State the blood parasite species.
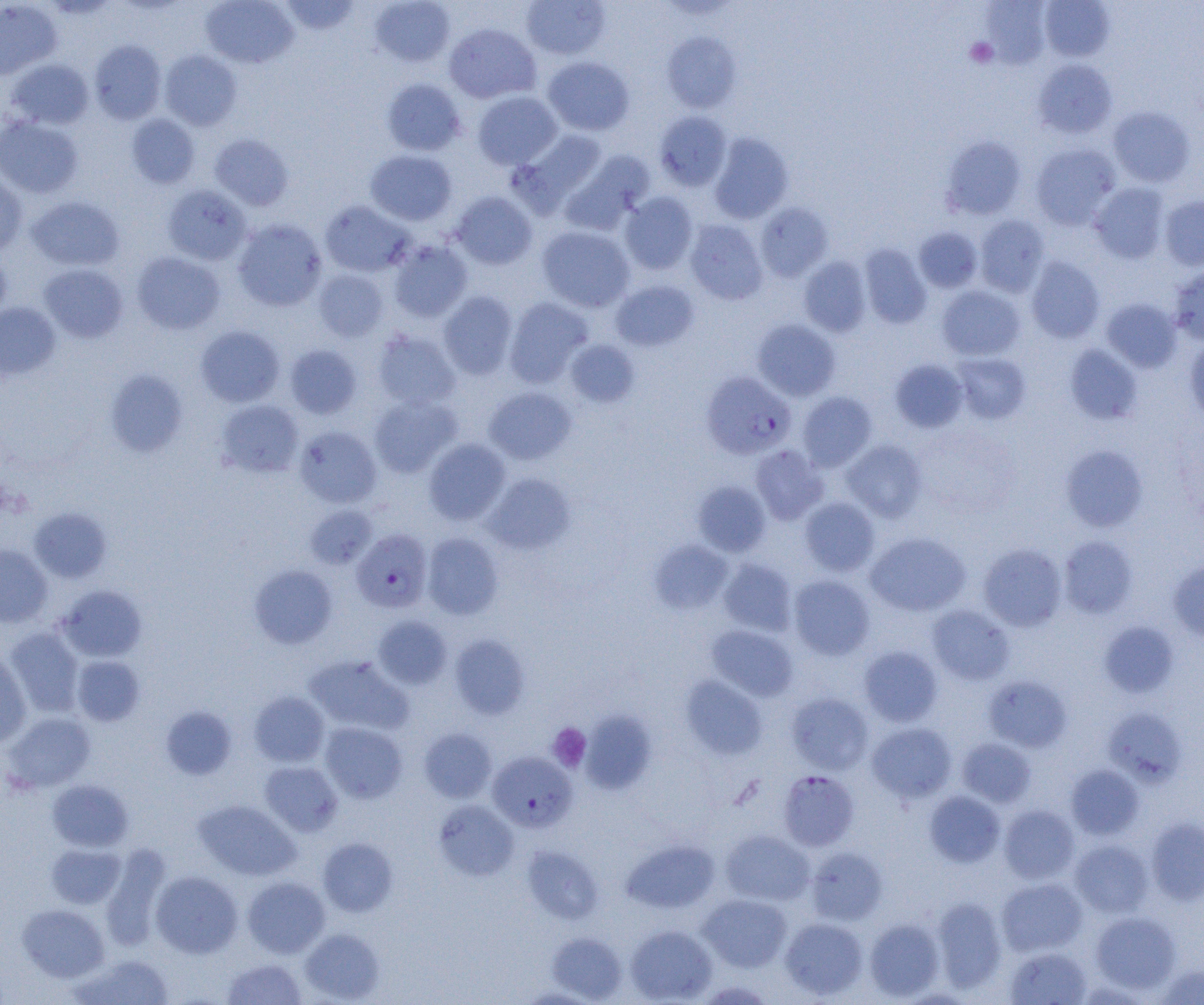

Plasmodium falciparum.

Approximate bounding boxes as (x1,y1)-(x2,y2) corner pairs in pixels. Uninfected red blood cell locations: (201,0)-(299,68), (280,0)-(360,36), (370,0)-(455,67), (521,0)-(611,60), (1039,0)-(1115,61), (0,1)-(61,79), (980,1)-(1052,69), (444,23)-(541,104), (662,31)-(741,113), (89,40)-(166,124), (159,50)-(242,130), (542,56)-(634,136), (5,58)-(94,130), (1033,59)-(1117,138), (381,78)-(466,156), (472,91)-(562,170), (1108,105)-(1195,187), (655,111)-(732,191), (126,113)-(200,189), (0,116)-(83,198), (515,128)-(608,209), (709,133)-(793,223), (210,134)-(293,211), (941,136)-(1026,219), (1030,144)-(1120,229), (365,149)-(457,226), (563,151)-(655,231), (0,171)-(27,255), (1089,183)-(1170,264), (162,184)-(251,265), (450,191)-(537,270), (619,191)-(698,275), (1160,195)-(1204,271), (26,196)-(124,272), (320,201)-(414,277), (755,202)-(833,282), (974,215)-(1050,296), (233,219)-(328,311), (685,219)-(768,305), (536,226)-(635,312), (913,226)-(983,293), (389,240)-(473,322), (859,243)-(931,328), (0,250)-(11,322), (132,252)-(225,335), (798,256)-(872,337), (1026,256)-(1104,343), (39,264)-(128,342), (1168,266)-(1204,345), (314,269)-(388,342), (610,279)-(699,352), (936,285)-(1025,361), (438,291)-(518,379), (504,297)-(593,387), (1101,298)-(1182,373), (0,302)-(61,380), (752,319)-(840,401), (196,325)-(284,407), (372,329)-(460,410), (1184,336)-(1204,422), (565,339)-(640,408), (285,344)-(363,419), (1064,344)-(1143,424), (951,353)-(1031,424), (890,360)-(968,433), (105,369)-(188,457), (483,387)-(577,465), (797,391)-(877,471), (369,394)-(461,477), (216,399)-(304,478), (294,425)-(382,508), (423,438)-(511,525), (841,439)-(927,522), (750,444)-(828,525), (1060,445)-(1148,532), (483,472)-(576,555), (693,480)-(771,557), (799,497)-(880,576), (304,504)-(378,569), (29,507)-(111,583), (422,532)-(504,620), (866,532)-(970,616), (1058,535)-(1137,618), (649,540)-(734,615), (979,543)-(1067,631), (0,544)-(52,627), (718,558)-(797,636), (1168,560)-(1204,643), (249,564)-(338,648), (788,575)-(875,660), (56,585)-(147,662), (927,604)-(1014,685), (373,616)-(452,689), (1099,621)-(1179,698), (707,625)-(798,701), (3,627)-(84,717), (449,634)-(530,720), (859,646)-(943,727), (0,653)-(32,746), (304,654)-(413,736), (73,655)-(144,726), (680,675)-(767,760), (983,676)-(1072,753), (249,691)-(329,767), (786,692)-(874,775), (161,706)-(237,780), (1103,708)-(1187,786), (581,709)-(656,794), (4,712)-(96,792), (866,721)-(957,802), (319,722)-(408,803), (418,727)-(497,803), (957,737)-(1036,807), (259,761)-(343,836), (1066,764)-(1144,839), (48,779)-(133,852), (924,790)-(1005,867), (194,799)-(301,881), (433,799)-(518,881), (999,805)-(1079,883), (1145,816)-(1204,904), (720,830)-(815,906), (318,838)-(397,917), (621,838)-(720,914), (1070,839)-(1153,917), (46,843)-(125,909), (522,846)-(604,923), (806,846)-(888,926), (100,847)-(171,950), (151,870)-(243,958), (243,876)-(330,958), (996,878)-(1087,956), (698,894)-(792,971), (931,896)-(1007,992), (18,904)-(109,982), (1090,911)-(1181,994), (780,917)-(868,1000), (864,918)-(944,1001), (625,924)-(717,1004), (300,927)-(384,1003), (546,932)-(627,1002), (1005,947)-(1092,1004), (71,954)-(175,1005), (222,957)-(306,1004), (1153,964)-(1204,1004), (515,987)-(603,1004). Plasmodium falciparum-infected red blood cell locations: (701,372)-(795,459), (352,529)-(433,612), (488,751)-(577,832), (778,770)-(859,851). Platelet locations: (965,37)-(998,68), (548,723)-(591,772). Image is 1204×1005 pixels. 1000x magnification. Optical microscopy. One field of a larger specimen. Thin blood film.